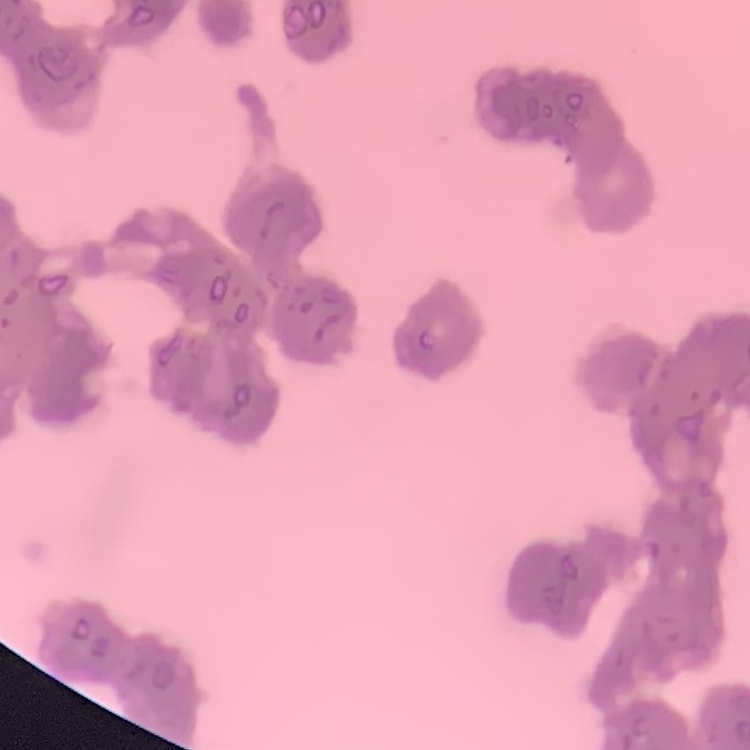

Summary:
  - Erythrocyte morphology: rouleaux formation
  - Preparation: thin blood smear
  - Image type: square crop of a larger photomicrograph
  - Stain: Field's or Giemsa